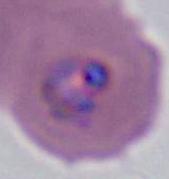

magnification = 400x or 1000x
modality = micrograph
identification = Plasmodium